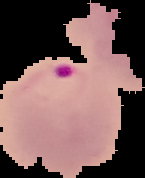
{
  "preparation": "thin blood smear",
  "malaria_status": "parasitized",
  "image_size": "145×178 pixels",
  "image_type": "segmented cell region with the area outside set to black"
}